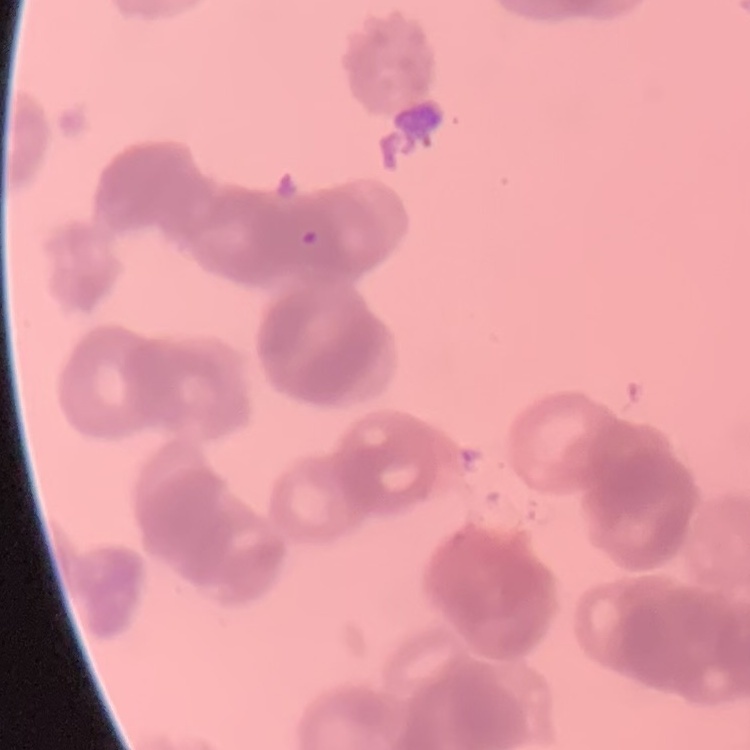
Summary:
  - Red blood cell morphology: rouleaux formation
  - Stain: Field's or Giemsa
  - Preparation: thin blood smear
  - Image type: square crop of a larger photomicrograph